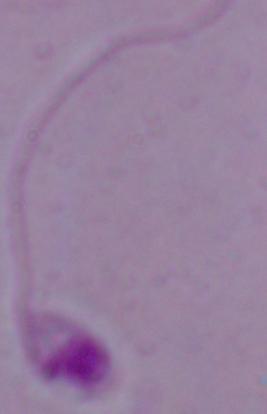

{
  "modality": "micrograph",
  "identification": "Leishmania",
  "magnification": "1000x"
}